Assess this cell for malaria.
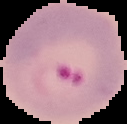
Parasitized.

image type = cell region segmented out of the field of view; surrounding area masked to black
preparation = thin blood film
image size = 127×124 pixels